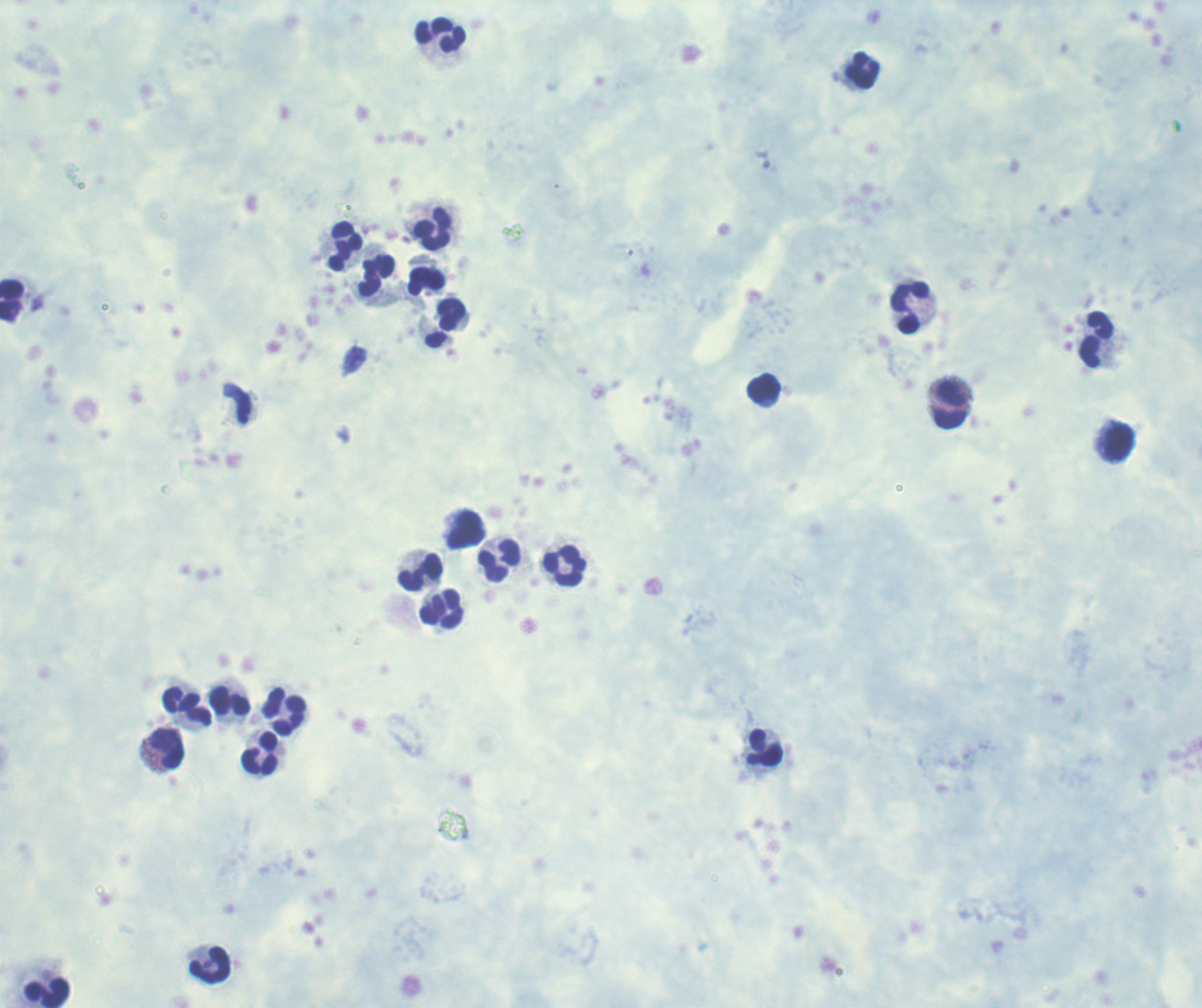
Approximate centers as [x, y] in pixels.
Summary:
  - Leukocyte locations: [441, 37], [862, 70], [432, 230], [346, 247], [377, 276], [426, 282], [11, 300], [910, 308], [451, 316], [1096, 340], [764, 389], [950, 406], [1119, 443], [466, 530], [500, 559], [564, 566], [421, 572], [442, 608], [231, 701], [188, 707], [285, 713], [167, 748], [765, 748], [260, 752], [209, 965], [47, 993]
  - Result: no Plasmodium parasites seen
  - Background quality: poor
  - Context: previously used in an actual diagnosis
  - Preparation: thick blood film
  - Image size: 1202×1008 pixels
  - Stain: Romanowsky
  - Field of view: one from this slide
  - Magnification: 100x